Locate every blood parasite and identify its species.
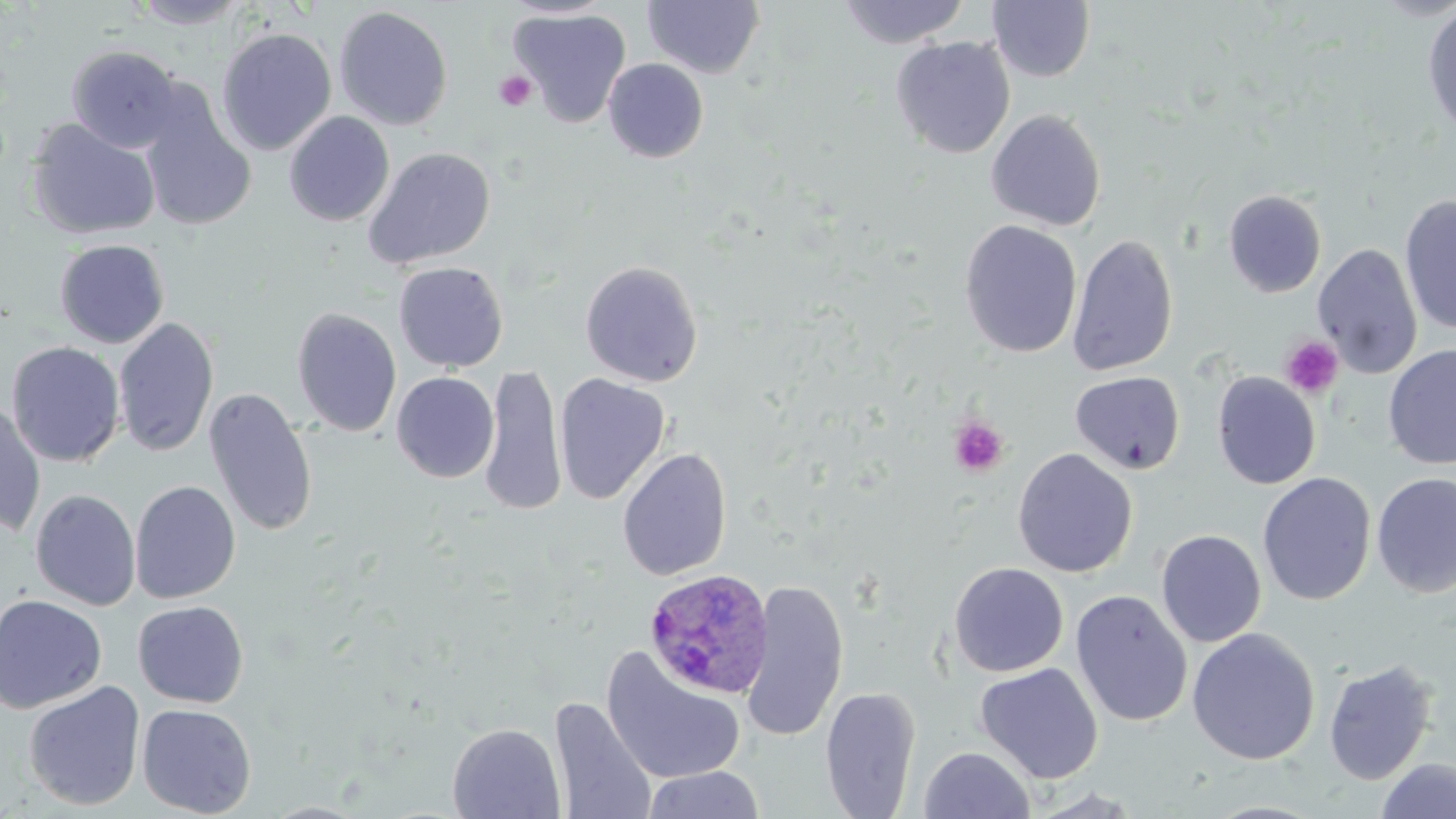
Approximate bounding boxes as named x1/y1/x2/y2 corners in pixels.
Plasmodium ovale-infected red blood cells: (x1=643, y1=569, x2=775, y2=699).
No Plasmodium falciparum, Plasmodium malariae, Plasmodium vivax, Babesia divergens, or Trypanosoma brucei observed.

Summary:
  - Platelet locations: (x1=494, y1=71, x2=536, y2=112), (x1=1280, y1=336, x2=1344, y2=400), (x1=948, y1=416, x2=1009, y2=477)
  - Uninfected red blood cell locations: (x1=838, y1=0, x2=970, y2=48), (x1=130, y1=1, x2=251, y2=29), (x1=642, y1=1, x2=765, y2=78), (x1=987, y1=1, x2=1095, y2=82), (x1=1422, y1=2, x2=1456, y2=140), (x1=334, y1=6, x2=453, y2=130), (x1=512, y1=8, x2=631, y2=128), (x1=216, y1=26, x2=337, y2=156), (x1=891, y1=36, x2=1015, y2=159), (x1=66, y1=44, x2=184, y2=153), (x1=604, y1=58, x2=709, y2=163), (x1=137, y1=90, x2=257, y2=232), (x1=986, y1=109, x2=1106, y2=231), (x1=978, y1=110, x2=1098, y2=353), (x1=284, y1=112, x2=395, y2=227), (x1=25, y1=118, x2=161, y2=240), (x1=364, y1=146, x2=497, y2=269), (x1=1223, y1=189, x2=1327, y2=298), (x1=1400, y1=194, x2=1456, y2=336), (x1=959, y1=220, x2=1083, y2=358), (x1=1067, y1=233, x2=1179, y2=377), (x1=54, y1=239, x2=169, y2=348), (x1=1313, y1=244, x2=1423, y2=380), (x1=580, y1=260, x2=704, y2=387), (x1=393, y1=261, x2=508, y2=372), (x1=292, y1=307, x2=402, y2=437), (x1=113, y1=318, x2=219, y2=457), (x1=6, y1=341, x2=125, y2=466), (x1=1383, y1=344, x2=1456, y2=469), (x1=482, y1=364, x2=566, y2=515), (x1=1070, y1=371, x2=1186, y2=475), (x1=1211, y1=371, x2=1321, y2=489), (x1=391, y1=372, x2=499, y2=483), (x1=554, y1=373, x2=671, y2=505), (x1=204, y1=387, x2=318, y2=537), (x1=0, y1=399, x2=46, y2=537), (x1=617, y1=447, x2=733, y2=581), (x1=1012, y1=448, x2=1138, y2=578), (x1=1257, y1=472, x2=1376, y2=606), (x1=1371, y1=472, x2=1456, y2=598), (x1=130, y1=480, x2=241, y2=604), (x1=30, y1=488, x2=142, y2=610), (x1=1155, y1=529, x2=1266, y2=648), (x1=948, y1=561, x2=1069, y2=677), (x1=739, y1=579, x2=849, y2=742), (x1=1070, y1=590, x2=1193, y2=728), (x1=0, y1=594, x2=107, y2=714), (x1=133, y1=600, x2=249, y2=708), (x1=1186, y1=627, x2=1321, y2=765), (x1=601, y1=647, x2=747, y2=785), (x1=1323, y1=659, x2=1438, y2=785), (x1=974, y1=663, x2=1103, y2=784), (x1=23, y1=680, x2=146, y2=811), (x1=820, y1=686, x2=921, y2=818), (x1=550, y1=696, x2=657, y2=819), (x1=137, y1=703, x2=257, y2=816), (x1=447, y1=723, x2=566, y2=819), (x1=919, y1=746, x2=1035, y2=819), (x1=1375, y1=757, x2=1456, y2=819), (x1=641, y1=766, x2=765, y2=819)
  - Slide-level diagnosis: Plasmodium ovale
  - Image size: 1456×819 pixels
  - Preparation: thin blood film
  - Stain: May-Grünwald-Giemsa
  - Modality: light microscopy
  - Field of view: single
  - Magnification: 1000x